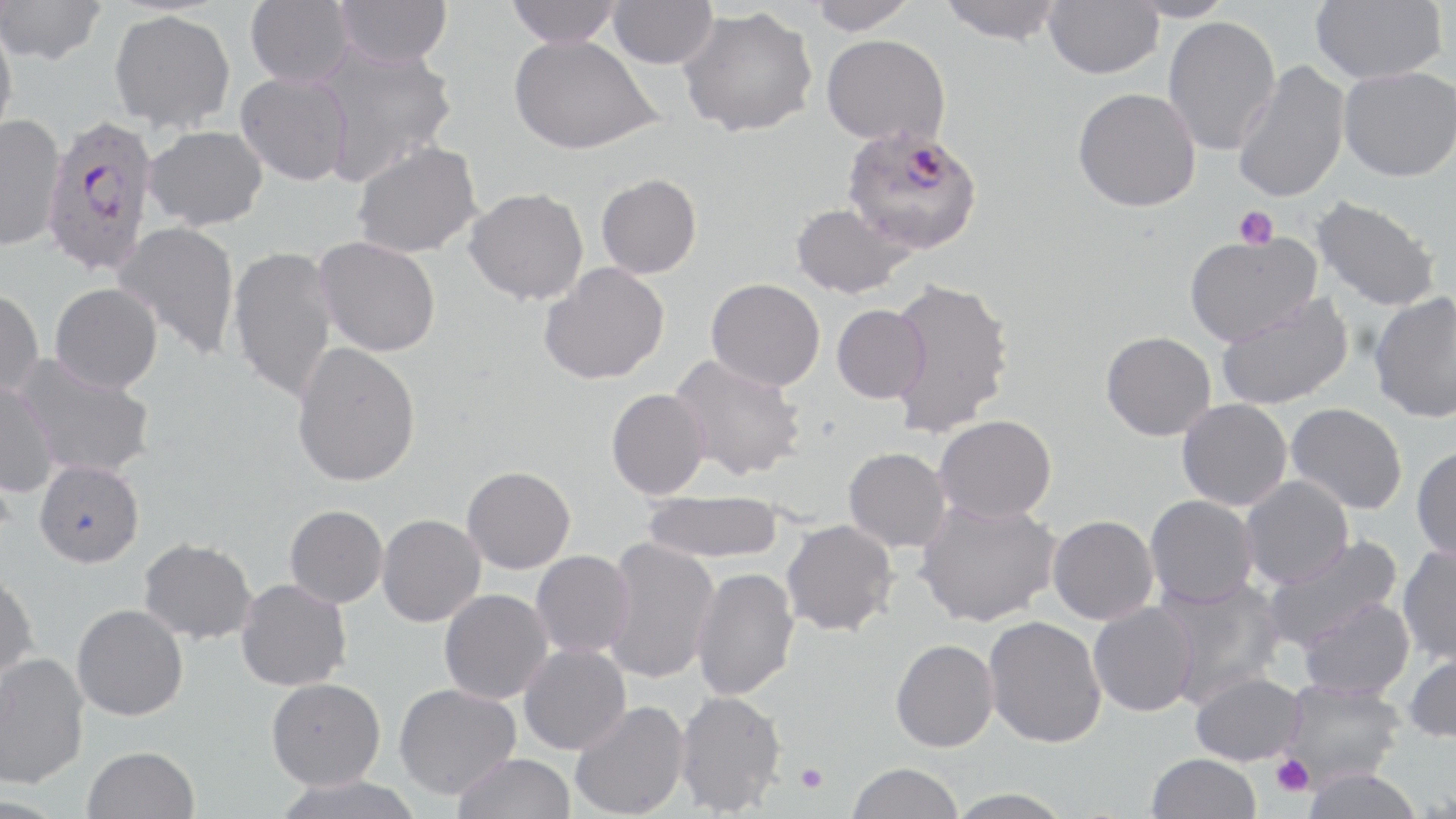
slide_level_diagnosis: Plasmodium falciparum
uninfected_red_blood_cell_locations: 'approximate bounding boxes as named x1/y1/x2/y2 corners in pixels: (x1=245, y1=0, x2=356, y2=88), (x1=335, y1=0, x2=452, y2=67), (x1=505, y1=0, x2=622, y2=47), (x1=607, y1=0, x2=716, y2=69), (x1=808, y1=0, x2=919, y2=35), (x1=938, y1=0, x2=1066, y2=45), (x1=1043, y1=0, x2=1163, y2=79), (x1=1124, y1=0, x2=1236, y2=23), (x1=1310, y1=0, x2=1446, y2=83), (x1=0, y1=1, x2=106, y2=66), (x1=678, y1=6, x2=818, y2=138), (x1=109, y1=9, x2=236, y2=134), (x1=0, y1=16, x2=18, y2=146), (x1=1162, y1=16, x2=1281, y2=156), (x1=508, y1=34, x2=662, y2=154), (x1=821, y1=34, x2=950, y2=146), (x1=311, y1=40, x2=459, y2=185), (x1=1231, y1=60, x2=1350, y2=204), (x1=1338, y1=66, x2=1456, y2=182), (x1=235, y1=72, x2=353, y2=185), (x1=1072, y1=86, x2=1201, y2=212), (x1=0, y1=113, x2=66, y2=252), (x1=144, y1=125, x2=268, y2=230), (x1=351, y1=140, x2=483, y2=258), (x1=596, y1=173, x2=702, y2=279), (x1=464, y1=187, x2=589, y2=305), (x1=1310, y1=194, x2=1442, y2=312), (x1=789, y1=202, x2=914, y2=299), (x1=112, y1=220, x2=241, y2=360), (x1=1183, y1=230, x2=1322, y2=345), (x1=314, y1=236, x2=441, y2=357), (x1=228, y1=244, x2=339, y2=405), (x1=538, y1=262, x2=669, y2=385), (x1=886, y1=277, x2=1015, y2=437), (x1=705, y1=278, x2=825, y2=391), (x1=50, y1=282, x2=163, y2=393), (x1=0, y1=287, x2=44, y2=398), (x1=1368, y1=291, x2=1456, y2=423), (x1=1215, y1=292, x2=1354, y2=410), (x1=831, y1=304, x2=930, y2=403), (x1=1100, y1=331, x2=1217, y2=441), (x1=291, y1=342, x2=421, y2=487), (x1=668, y1=353, x2=807, y2=481), (x1=14, y1=354, x2=157, y2=480), (x1=0, y1=379, x2=59, y2=497), (x1=606, y1=388, x2=710, y2=499), (x1=1176, y1=398, x2=1292, y2=511), (x1=1286, y1=403, x2=1407, y2=515), (x1=933, y1=414, x2=1056, y2=523), (x1=1411, y1=446, x2=1456, y2=562), (x1=843, y1=447, x2=951, y2=552), (x1=34, y1=459, x2=144, y2=568), (x1=461, y1=465, x2=575, y2=573), (x1=1240, y1=475, x2=1354, y2=588), (x1=640, y1=491, x2=784, y2=563), (x1=1144, y1=495, x2=1259, y2=608), (x1=913, y1=497, x2=1061, y2=627), (x1=284, y1=504, x2=388, y2=607), (x1=376, y1=514, x2=486, y2=627), (x1=1047, y1=514, x2=1159, y2=624), (x1=780, y1=519, x2=899, y2=637), (x1=1262, y1=535, x2=1403, y2=653), (x1=138, y1=537, x2=257, y2=644), (x1=602, y1=537, x2=719, y2=684), (x1=1397, y1=543, x2=1456, y2=665), (x1=530, y1=550, x2=634, y2=659), (x1=691, y1=566, x2=800, y2=701), (x1=0, y1=569, x2=40, y2=688), (x1=1154, y1=575, x2=1286, y2=708), (x1=235, y1=578, x2=352, y2=691), (x1=439, y1=589, x2=552, y2=704), (x1=1297, y1=597, x2=1415, y2=700), (x1=1088, y1=602, x2=1198, y2=717), (x1=72, y1=603, x2=189, y2=721), (x1=983, y1=616, x2=1107, y2=748), (x1=890, y1=638, x2=999, y2=752), (x1=519, y1=644, x2=630, y2=754), (x1=1402, y1=646, x2=1456, y2=743), (x1=0, y1=652, x2=89, y2=789), (x1=1190, y1=670, x2=1305, y2=765), (x1=266, y1=677, x2=385, y2=789), (x1=1278, y1=678, x2=1407, y2=786), (x1=394, y1=683, x2=521, y2=799), (x1=674, y1=689, x2=787, y2=816), (x1=569, y1=700, x2=690, y2=818), (x1=82, y1=746, x2=199, y2=819), (x1=452, y1=752, x2=576, y2=819), (x1=1147, y1=753, x2=1261, y2=819), (x1=846, y1=762, x2=964, y2=819), (x1=1301, y1=766, x2=1424, y2=819), (x1=271, y1=775, x2=425, y2=819), (x1=943, y1=787, x2=1077, y2=818)'
plasmodium_falciparum_infected_red_blood_cell_locations: 'approximate bounding boxes as named x1/y1/x2/y2 corners in pixels: (x1=41, y1=116, x2=158, y2=275), (x1=841, y1=125, x2=985, y2=255)'
preparation: thin blood film
stain: May-Grünwald-Giemsa
modality: optical microscopy
field_of_view: single
image_size: 1456×819 pixels
magnification: 1000x
platelet_locations: 'approximate bounding boxes as named x1/y1/x2/y2 corners in pixels: (x1=1234, y1=205, x2=1278, y2=249), (x1=1270, y1=753, x2=1314, y2=798), (x1=795, y1=763, x2=829, y2=793)'